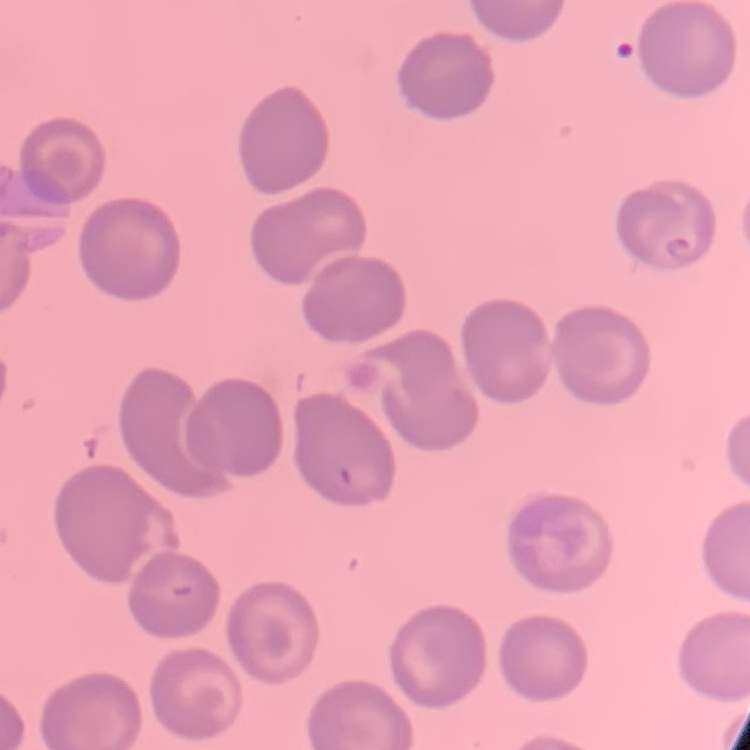

The red blood cells exhibit no rouleaux formation. Thin blood film. One tile cut from a larger photomicrograph. Stained with either Field's or Giemsa.